Report the malaria status of this cell.
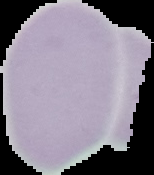
Uninfected.

Summary:
  - Image type: cell region segmented out of the field of view; surrounding area masked to black
  - Preparation: thin blood film
  - Image size: 154×175 pixels